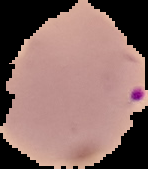

Summary:
  - Image size: 148×169 pixels
  - Image type: segmented cell region with the area outside set to black
  - Preparation: thin blood film
  - Malaria status: parasitized